Identify the preparation type.
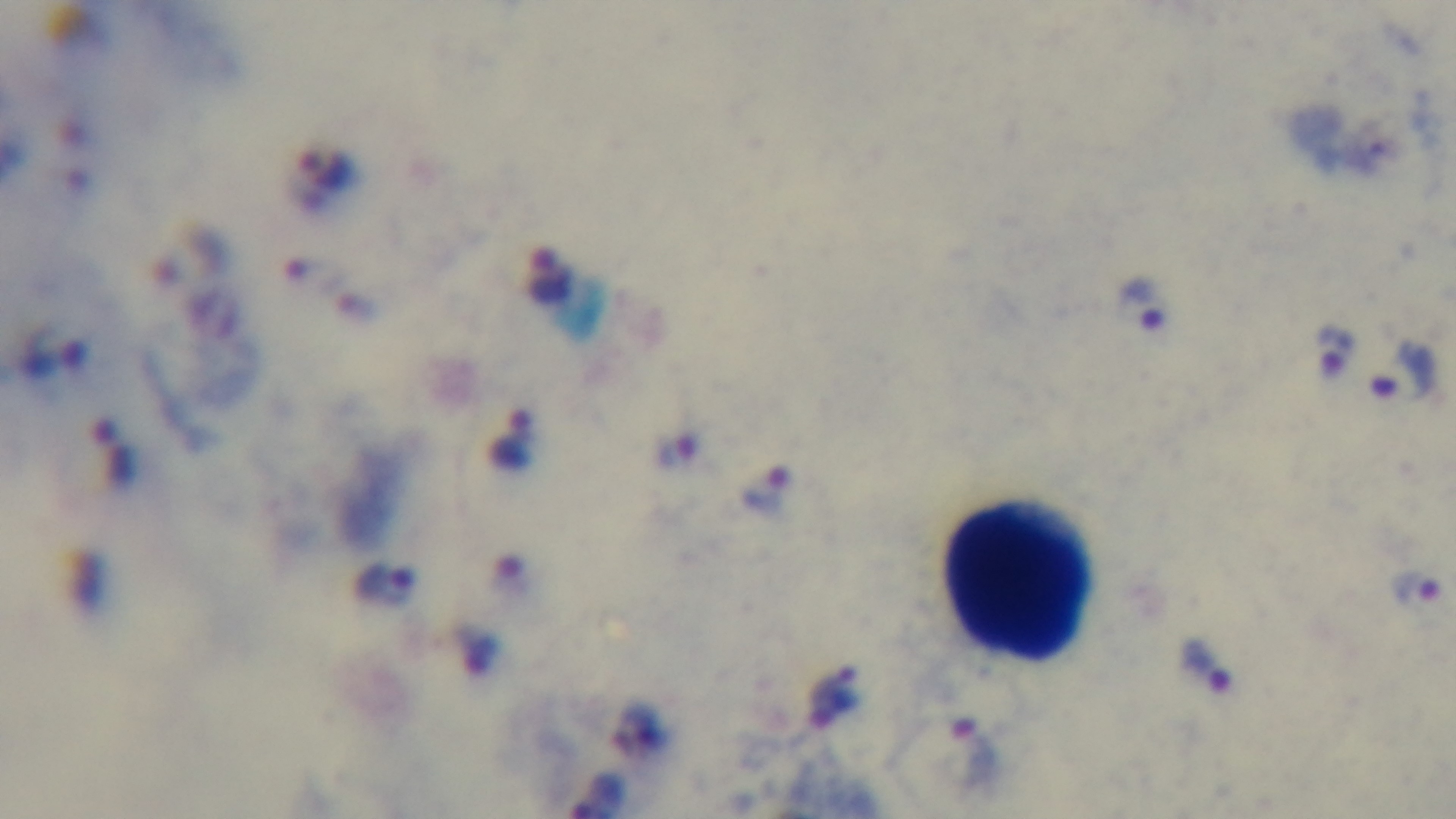

Thick.

Summary:
  - Field of view: single
  - Capture: mounted 4K digital camera
  - Stain: Giemsa
  - Modality: light microscopy
  - Malaria status: positive
  - Objective: 100x oil immersion